State which parasite is depicted.
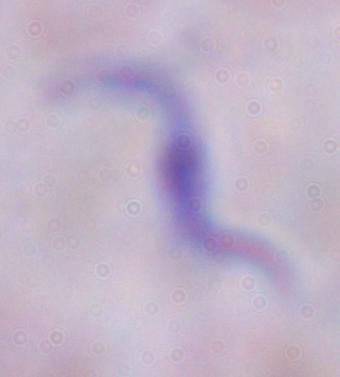
A trypanosome.

Captured at 1000x magnification. Photomicrograph.